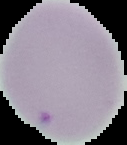
preparation = thin blood film
result = negative for malaria parasites
image type = segmented cell region on a black background
image size = 127×145 pixels